Outline each blood parasite and name the species.
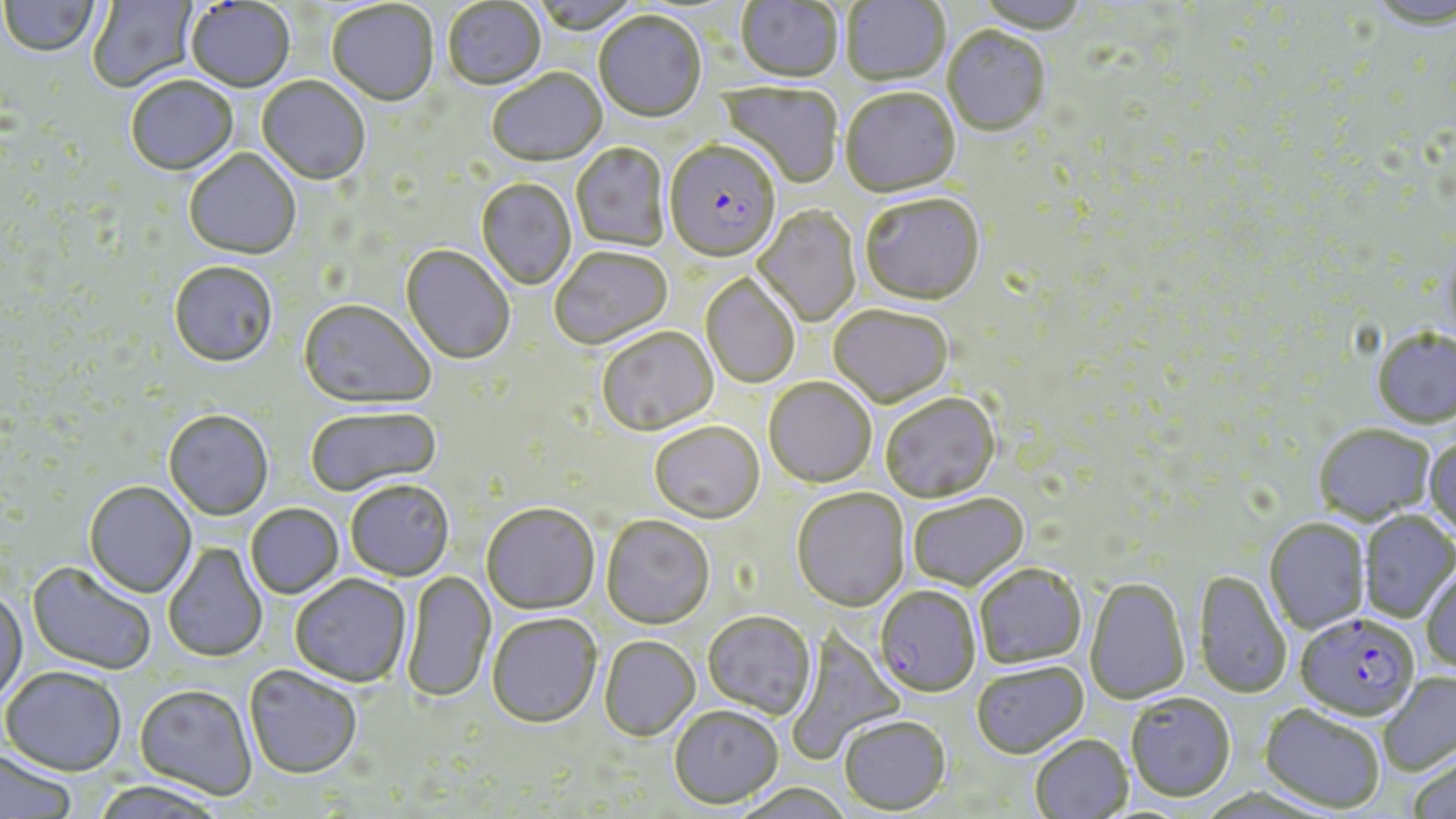
Approximate bounding boxes as (x1, y1, x2, y2) in pixels.
Plasmodium falciparum-infected red blood cells: (664, 142, 782, 265), (874, 584, 981, 697), (1295, 614, 1420, 723).
No Plasmodium ovale, Plasmodium malariae, Plasmodium vivax, Babesia divergens, or Trypanosoma brucei observed.

Uninfected red blood cell locations: (87, 0, 200, 94), (527, 0, 643, 35), (736, 0, 843, 84), (842, 0, 950, 87), (972, 0, 1091, 35), (1, 1, 100, 59), (185, 1, 295, 94), (442, 1, 547, 92), (327, 2, 439, 108), (1368, 2, 1456, 30), (593, 13, 707, 125), (942, 28, 1050, 138), (487, 70, 608, 169), (126, 77, 238, 178), (256, 78, 370, 187), (717, 82, 844, 189), (841, 89, 960, 199), (571, 144, 670, 252), (184, 151, 301, 261), (476, 179, 576, 290), (859, 196, 985, 308), (753, 206, 861, 327), (400, 246, 515, 366), (550, 247, 674, 352), (169, 263, 278, 370), (700, 274, 800, 389), (298, 301, 435, 411), (828, 306, 953, 408), (596, 329, 719, 437), (1371, 329, 1456, 429), (764, 378, 876, 488), (880, 393, 1000, 503), (305, 407, 442, 498), (163, 411, 273, 522), (649, 422, 765, 524), (1313, 425, 1435, 526), (1424, 435, 1456, 539), (345, 481, 454, 582), (84, 482, 197, 599), (791, 488, 910, 611), (908, 494, 1029, 591), (246, 504, 344, 600), (481, 504, 600, 615), (1359, 510, 1456, 623), (601, 516, 715, 630), (1264, 519, 1370, 634), (162, 542, 268, 663), (27, 562, 156, 675), (974, 563, 1086, 669), (1420, 564, 1456, 675), (401, 571, 496, 703), (1193, 571, 1293, 699), (290, 574, 412, 689), (1084, 578, 1190, 705), (0, 591, 28, 705), (702, 611, 816, 719), (486, 615, 602, 729), (783, 630, 905, 765), (600, 637, 700, 742), (971, 661, 1089, 759), (243, 665, 362, 780), (1, 667, 127, 777), (1378, 672, 1456, 776), (134, 684, 256, 800), (1125, 694, 1236, 804), (669, 705, 784, 809), (1258, 705, 1385, 815), (839, 716, 951, 815), (1030, 735, 1133, 819), (0, 750, 77, 819), (1408, 754, 1456, 819), (91, 781, 227, 819), (731, 782, 854, 819). Slide-level diagnosis: Plasmodium falciparum. May-Grünwald-Giemsa stain. 1000x magnification. Light microscopy. One field of a larger specimen. Thin blood smear. Image is 1456×819 pixels.